Assess this cell for malaria.
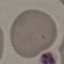
It is uninfected.

stain = Giemsa
preparation = thin blood film
capture = smartphone camera at the microscope eyepiece
image type = automatically extracted cell patch, resized to 64 × 64 pixels